Locate platelets.
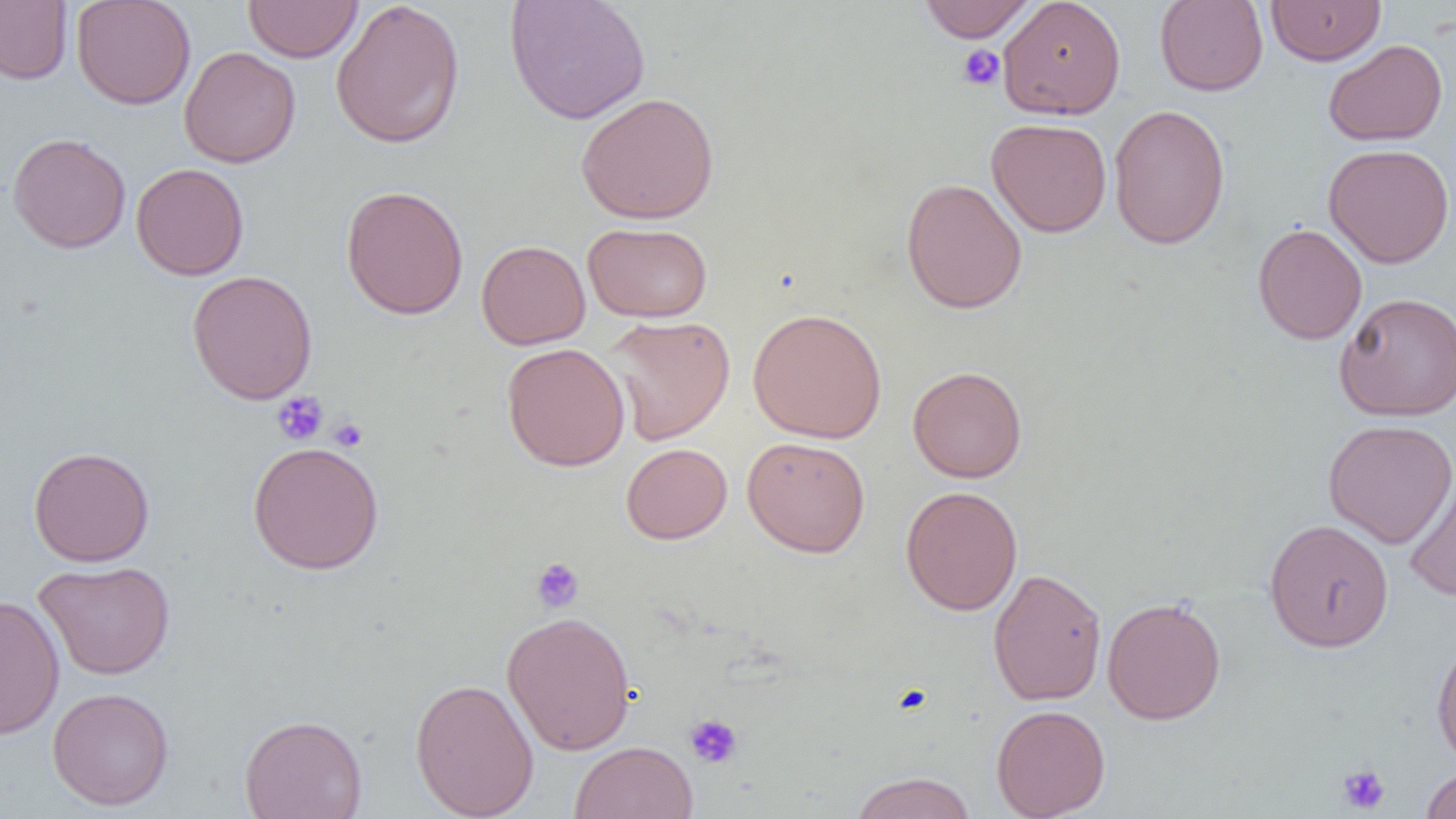
Approximate bounding boxes as (x1, y1, x2, y2) in pixels.
Platelets: (957, 44, 1005, 91), (271, 391, 329, 445), (328, 417, 367, 452), (530, 557, 584, 613), (684, 713, 743, 770), (1337, 764, 1390, 814), (1417, 764, 1456, 818).

Uninfected red blood cell locations: (71, 0, 196, 110), (504, 0, 651, 125), (917, 0, 1038, 42), (998, 0, 1126, 120), (1265, 0, 1386, 66), (0, 1, 72, 85), (243, 1, 362, 62), (329, 1, 466, 148), (1154, 1, 1268, 96), (1323, 39, 1449, 146), (178, 46, 301, 168), (575, 91, 720, 224), (1108, 103, 1231, 250), (986, 118, 1112, 237), (7, 133, 131, 253), (1323, 143, 1455, 269), (131, 162, 249, 280), (901, 177, 1028, 315), (340, 185, 469, 319), (582, 222, 713, 322), (1252, 223, 1367, 344), (476, 239, 591, 350), (187, 269, 318, 405), (1333, 291, 1456, 421), (747, 308, 887, 443), (603, 314, 735, 445), (501, 342, 630, 472), (907, 366, 1027, 483), (1323, 419, 1456, 548), (742, 436, 870, 558), (247, 440, 385, 575), (621, 442, 732, 544), (28, 446, 155, 567), (1403, 471, 1456, 602), (900, 485, 1023, 616), (1264, 518, 1394, 652), (33, 560, 176, 680), (987, 568, 1107, 706), (0, 594, 65, 740), (1101, 597, 1226, 725), (501, 611, 636, 755), (1431, 636, 1456, 768), (410, 677, 539, 819), (48, 687, 175, 811), (991, 703, 1110, 819), (239, 713, 367, 819), (570, 741, 698, 819), (1420, 765, 1456, 819), (850, 772, 976, 819). Slide-level diagnosis: no evidence of blood parasites. Image is 1456×819 pixels. Captured at 1000x magnification. Single field of view. Light microscopy. Thin blood smear.